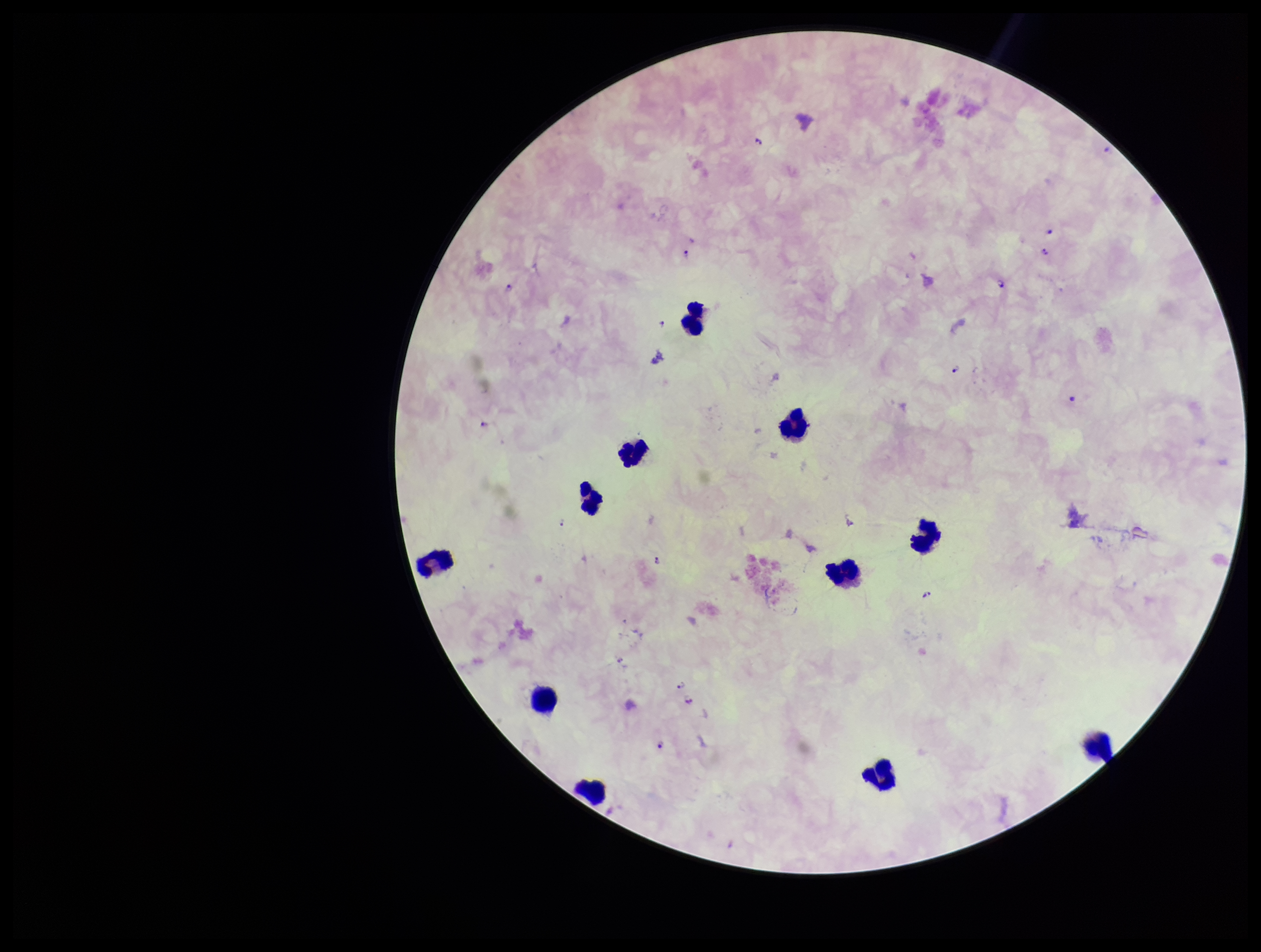

Patient malaria status: positive. Stained with Giemsa. Preparation: thick blood smear. Parasite count: 16. Single field of view. Smartphone photograph taken through the eyepiece of a microscope. Leukocyte count: 11. Plasmodium parasites: detected. Image is 1261×952 pixels. Species reported for this patient: Plasmodium falciparum.